State which parasite is depicted.
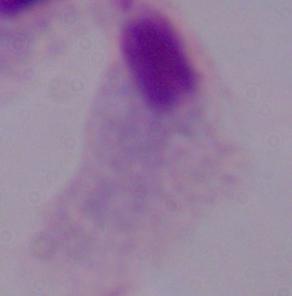
A trichomonad.

Summary:
  - Magnification: 1000x
  - Modality: photomicrograph